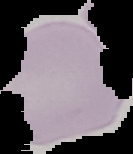
preparation: thin blood film
image_size: 133×154 pixels
malaria_status: uninfected
image_type: cell region segmented out of the field of view; surrounding area masked to black